Locate every blood parasite and identify its species.
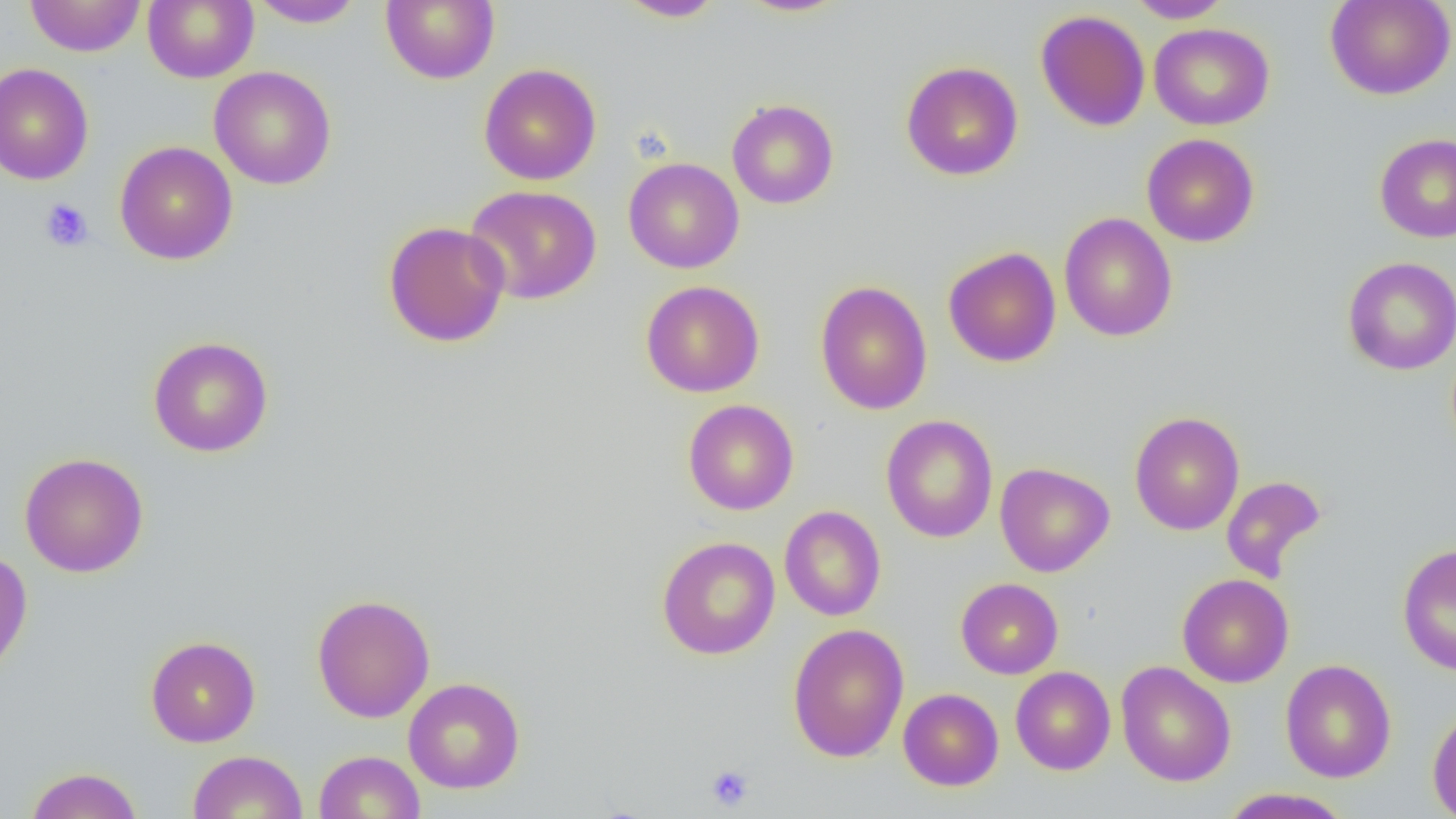
No blood parasites observed.

Approximate bounding boxes as named x1/y1/x2/y2 corners in pixels. Uninfected red blood cell locations: (x1=24, y1=0, x2=145, y2=57), (x1=143, y1=0, x2=258, y2=83), (x1=380, y1=0, x2=499, y2=85), (x1=617, y1=0, x2=727, y2=21), (x1=734, y1=0, x2=852, y2=18), (x1=1125, y1=0, x2=1232, y2=23), (x1=1324, y1=0, x2=1455, y2=100), (x1=249, y1=1, x2=366, y2=28), (x1=1035, y1=9, x2=1150, y2=132), (x1=1149, y1=22, x2=1275, y2=130), (x1=901, y1=61, x2=1023, y2=181), (x1=0, y1=62, x2=94, y2=185), (x1=478, y1=63, x2=602, y2=186), (x1=209, y1=66, x2=337, y2=190), (x1=727, y1=98, x2=839, y2=209), (x1=1141, y1=133, x2=1259, y2=247), (x1=1374, y1=133, x2=1456, y2=243), (x1=114, y1=141, x2=238, y2=265), (x1=623, y1=157, x2=744, y2=274), (x1=465, y1=184, x2=602, y2=305), (x1=1059, y1=212, x2=1177, y2=342), (x1=382, y1=220, x2=511, y2=347), (x1=943, y1=247, x2=1061, y2=368), (x1=1342, y1=256, x2=1456, y2=375), (x1=640, y1=280, x2=765, y2=397), (x1=814, y1=281, x2=933, y2=415), (x1=148, y1=335, x2=274, y2=458), (x1=683, y1=399, x2=799, y2=515), (x1=1129, y1=410, x2=1245, y2=536), (x1=881, y1=415, x2=998, y2=542), (x1=19, y1=452, x2=149, y2=577), (x1=995, y1=462, x2=1114, y2=577), (x1=1221, y1=475, x2=1327, y2=583), (x1=779, y1=505, x2=886, y2=621), (x1=656, y1=535, x2=780, y2=659), (x1=1397, y1=543, x2=1456, y2=676), (x1=0, y1=549, x2=33, y2=681), (x1=1177, y1=573, x2=1293, y2=688), (x1=956, y1=578, x2=1063, y2=679), (x1=311, y1=593, x2=436, y2=723), (x1=787, y1=623, x2=909, y2=762), (x1=145, y1=635, x2=261, y2=747), (x1=1280, y1=658, x2=1396, y2=783), (x1=1116, y1=661, x2=1236, y2=787), (x1=1011, y1=666, x2=1115, y2=775), (x1=403, y1=677, x2=525, y2=793), (x1=898, y1=688, x2=1003, y2=791), (x1=1427, y1=705, x2=1456, y2=818), (x1=188, y1=750, x2=308, y2=819), (x1=313, y1=750, x2=426, y2=818), (x1=24, y1=766, x2=143, y2=819), (x1=1218, y1=787, x2=1354, y2=819). Platelet locations: (x1=40, y1=198, x2=93, y2=252), (x1=705, y1=764, x2=755, y2=811). Slide-level diagnosis: negative for blood parasites. Image is 1456×819 pixels. 1000x magnification. Optical microscopy. One field of a larger specimen. Thin blood film.